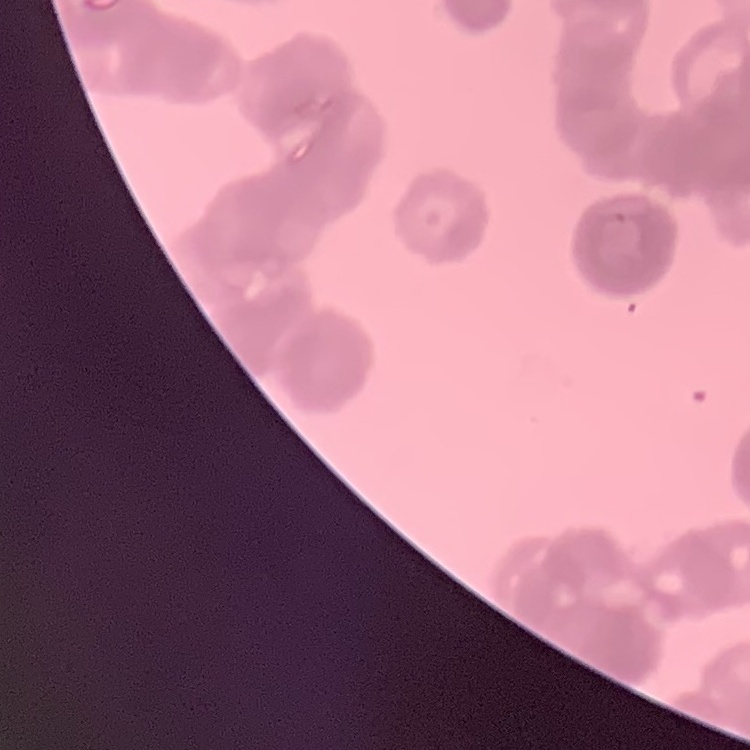

The erythrocytes show rouleaux formation. Square crop of a larger photomicrograph. Stained with either Field's or Giemsa. Thin blood film.